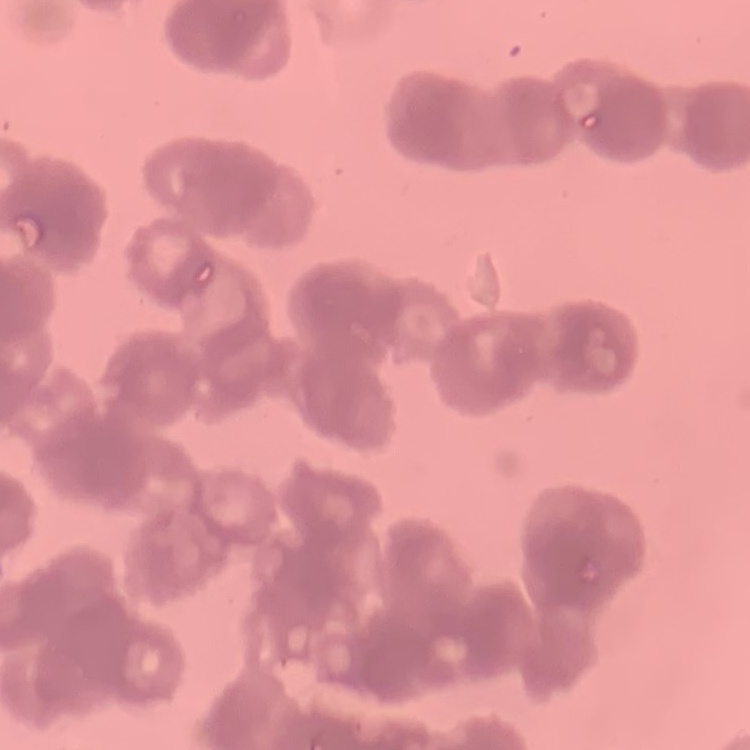

Summary:
  - Erythrocyte morphology: rouleaux formation
  - Stain: Field's or Giemsa
  - Image type: one tile cut from a larger photomicrograph
  - Preparation: thin peripheral smear